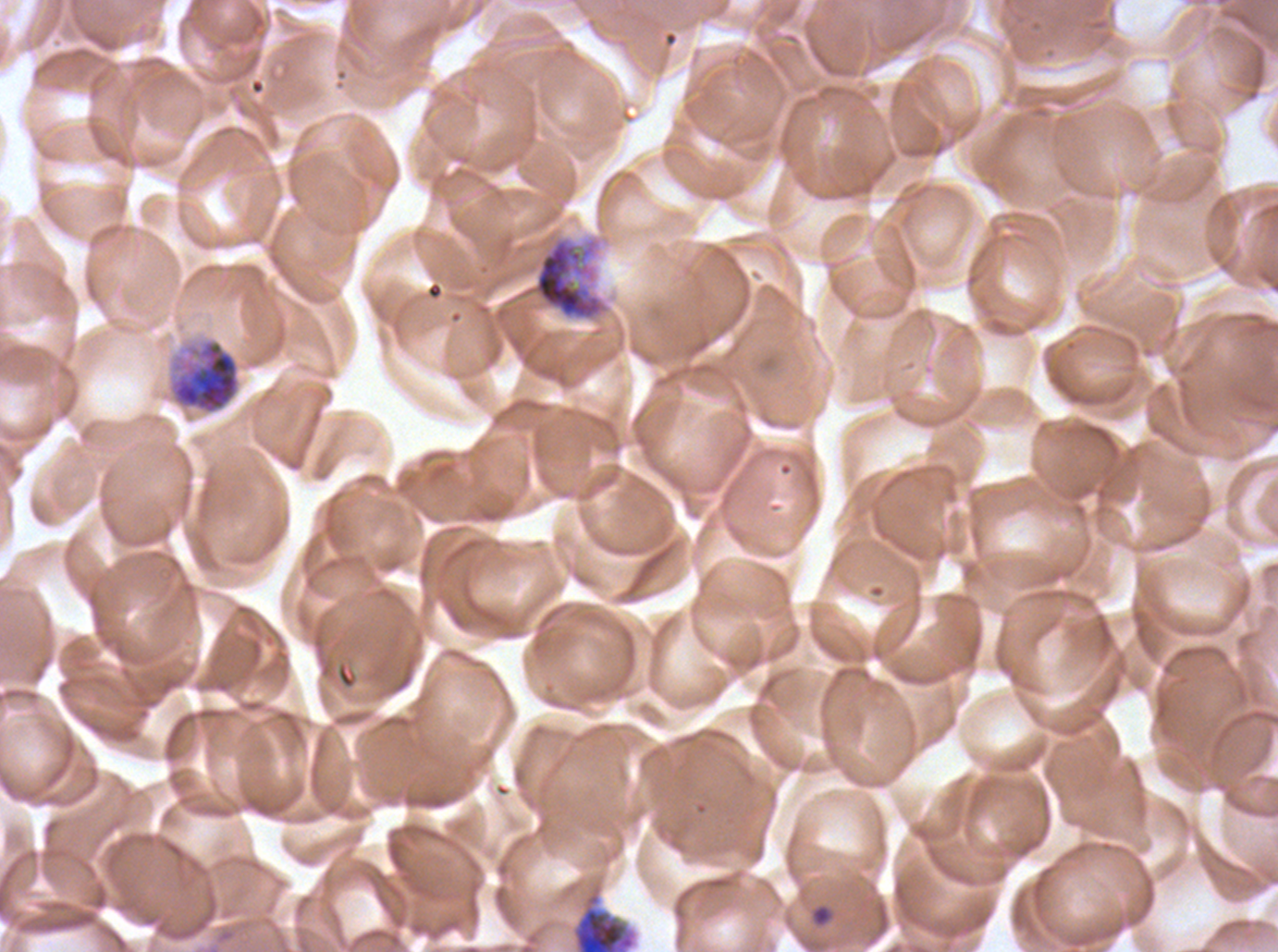
Approximate bounding rectangles given as corner coordinates in pixels from the top-left. Debris locations: (x1=570, y1=881, x2=639, y2=951). Ring locations: (x1=810, y1=904, x2=832, y2=927). Segmenter locations: (x1=518, y1=236, x2=608, y2=322), (x1=166, y1=336, x2=242, y2=416). Thin blood film. Life-cycle stages observed: ring, segmenter. Giemsa stain. Image is 1278×952 pixels. Plasmodium falciparum from a patient in The Gambia, cultured ex vivo for 24 to 48 hours. A sub-image separated from a larger composite.